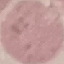
malaria_status: uninfected
image_type: cell patch, automatically extracted from a larger field of view and resized to 64 × 64 pixels
preparation: thin smear
stain: Giemsa
capture: smartphone camera at the microscope eyepiece